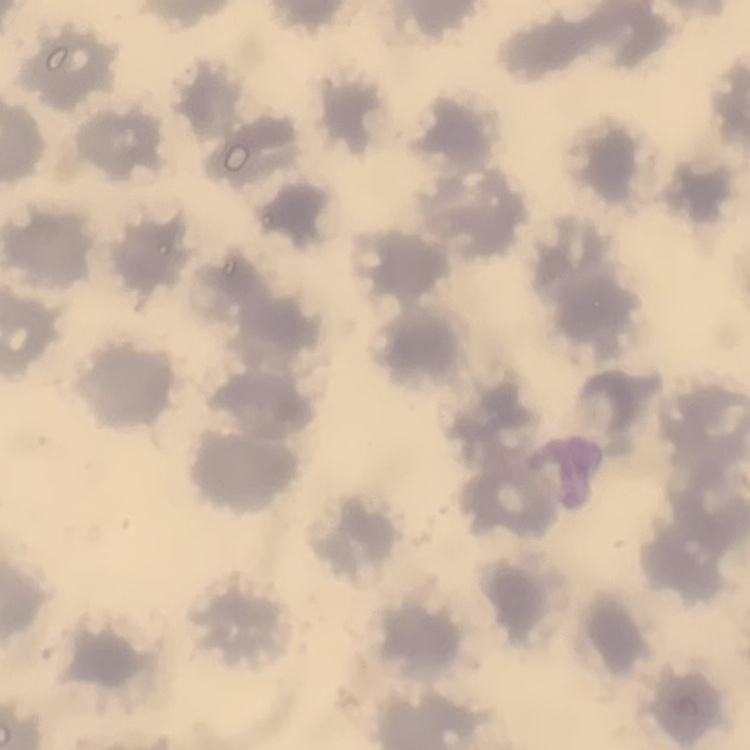

erythrocyte morphology = no rouleaux formation
preparation = thin blood film
image type = square crop of a larger photomicrograph
stain = Field's or Giemsa